Outline each Plasmodium vivax-infected red blood cell.
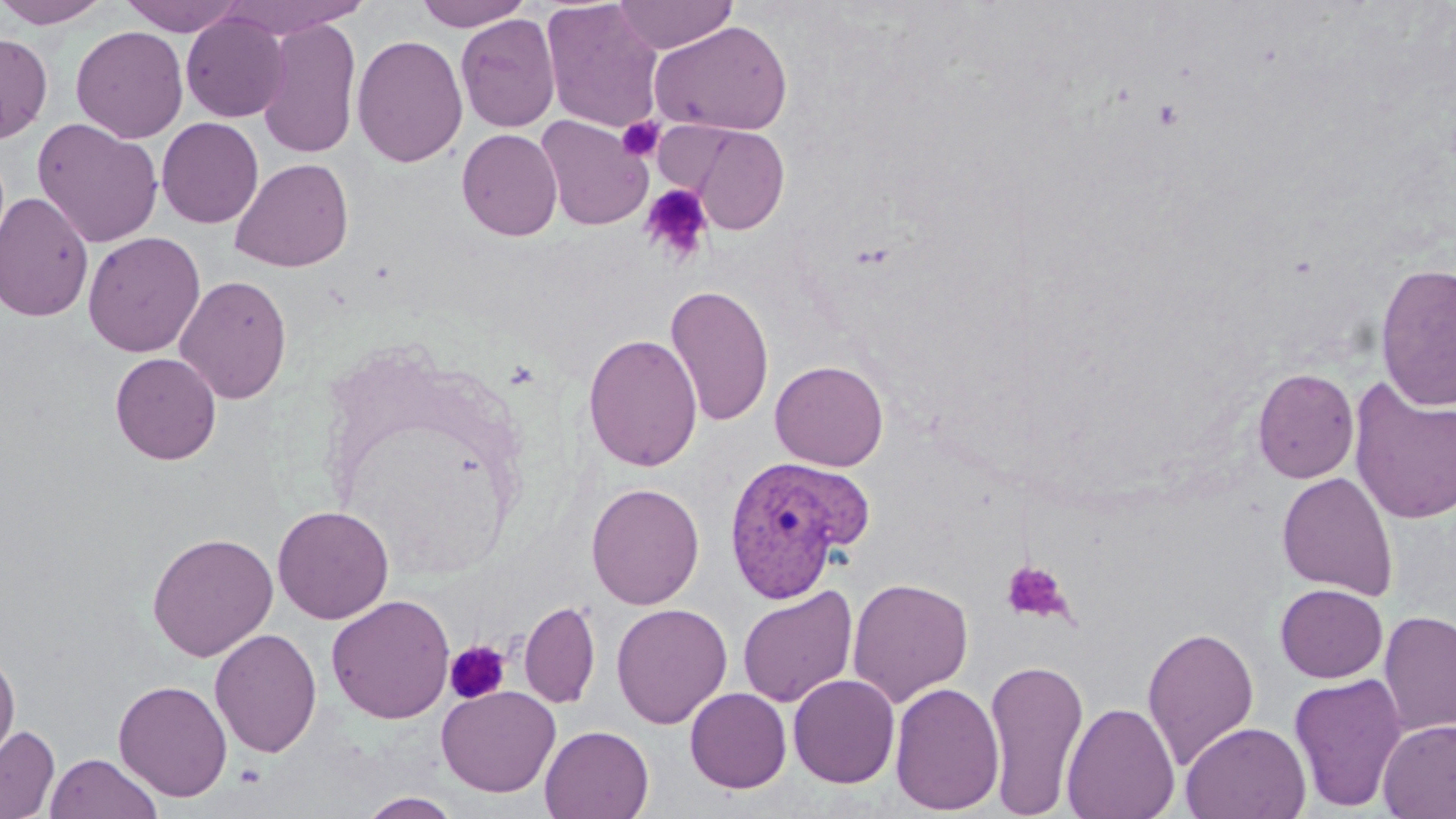
Approximate bounding boxes as (x1,y1)-(x2,y2) corner pairs in pixels.
Plasmodium vivax-infected red blood cells: (722,456)-(863,604).

Platelet locations: (1152,99)-(1185,130), (618,117)-(664,162), (639,183)-(713,265), (1001,560)-(1073,624), (444,640)-(511,705). Uninfected red blood cell locations: (0,0)-(112,28), (119,0)-(247,36), (223,0)-(370,38), (415,0)-(531,31), (541,0)-(665,134), (613,0)-(738,54), (181,12)-(289,122), (455,14)-(560,132), (257,16)-(362,160), (651,19)-(793,135), (71,25)-(189,143), (0,31)-(53,143), (352,34)-(468,168), (536,115)-(653,231), (156,117)-(264,229), (32,118)-(163,248), (678,123)-(789,235), (457,128)-(563,241), (230,157)-(354,272), (0,192)-(94,322), (83,231)-(205,358), (1374,263)-(1456,412), (175,274)-(293,404), (664,284)-(775,428), (583,333)-(703,473), (110,352)-(221,464), (770,359)-(889,471), (1252,368)-(1359,483), (1349,377)-(1456,526), (1277,472)-(1398,600), (586,482)-(704,610), (273,505)-(394,624), (146,531)-(278,661), (847,576)-(973,708), (1275,584)-(1387,682), (737,585)-(858,708), (326,595)-(455,724), (519,600)-(600,709), (611,602)-(732,729), (1378,610)-(1456,738), (1142,625)-(1259,769), (209,628)-(322,758), (0,647)-(20,769), (982,657)-(1090,815), (1288,673)-(1409,812), (788,674)-(900,788), (114,679)-(232,801), (889,681)-(1005,815), (436,686)-(560,797), (685,688)-(791,793), (1061,702)-(1180,819), (1378,718)-(1456,818), (1181,721)-(1311,819), (0,725)-(59,818), (540,725)-(654,819), (45,752)-(163,819), (359,791)-(462,819). Slide-level diagnosis: Plasmodium vivax. May-Grünwald-Giemsa stain. Optical microscopy. Single field of view. Thin blood smear. Image is 1456×819 pixels. Captured at 1000x magnification.